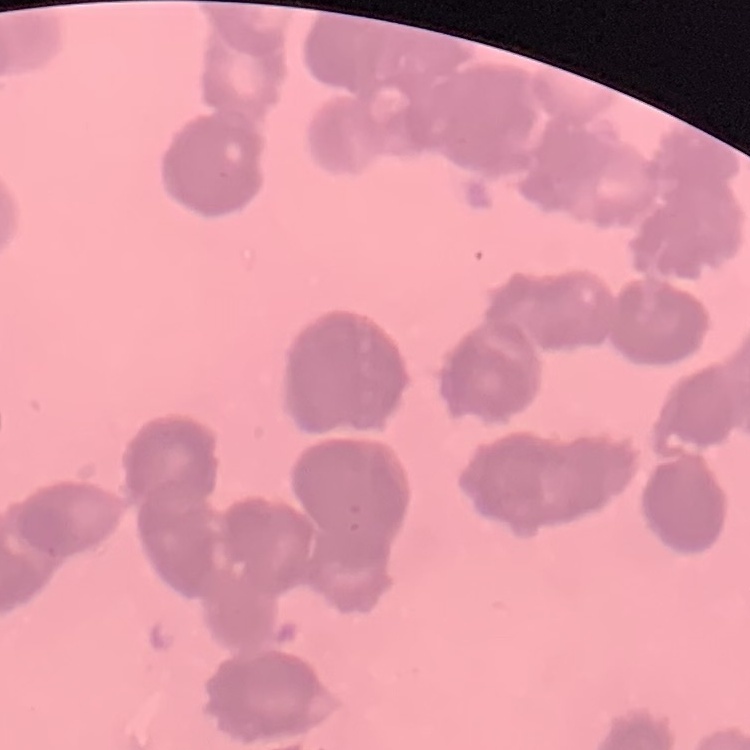

The red blood cells show rouleaux formation. Square crop of a larger photomicrograph. Field's or Giemsa stain. Thin blood smear.